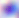
400x magnification. Micrograph. Toxoplasma gondii is seen.